Outline each blood parasite and name the species.
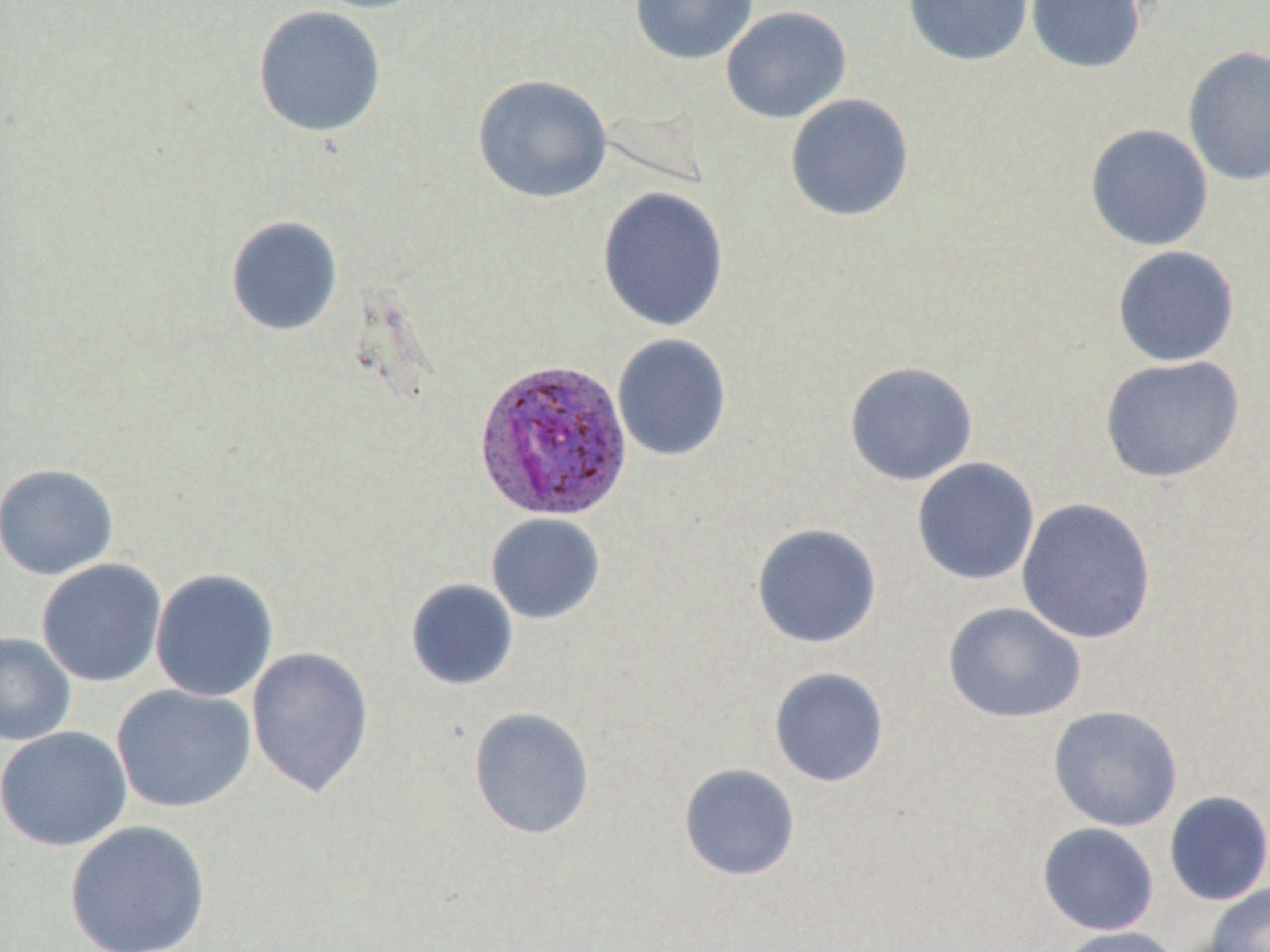
Approximate bounding boxes as [x1, y1, x2, y2] in pixels.
Plasmodium ovale-infected red blood cells: [472, 357, 635, 522].
No Plasmodium falciparum, Plasmodium malariae, Plasmodium vivax, Babesia divergens, or Trypanosoma brucei observed.

slide-level diagnosis = Plasmodium ovale
preparation = thin blood smear
magnification = 1000x
image size = 1270×952 pixels
field of view = one of a larger specimen
uninfected red blood cell locations = approximate bounding boxes as [x1, y1, x2, y2] in pixels: [306, 0, 434, 13], [630, 0, 758, 65], [903, 0, 1035, 67], [1025, 0, 1146, 74], [252, 5, 388, 138], [721, 6, 852, 124], [1183, 45, 1270, 186], [472, 73, 613, 204], [784, 93, 915, 223], [1084, 123, 1214, 252], [597, 185, 730, 332], [225, 214, 344, 337], [1112, 245, 1240, 367], [612, 333, 733, 462], [1099, 355, 1245, 483], [844, 361, 978, 486], [911, 457, 1041, 586], [0, 463, 119, 580], [1016, 497, 1157, 644], [485, 513, 606, 625], [751, 523, 882, 649], [36, 558, 167, 687], [150, 568, 279, 703], [404, 578, 520, 692], [942, 602, 1087, 724], [0, 632, 77, 746], [246, 646, 375, 798], [768, 667, 890, 788], [111, 683, 256, 813], [1048, 705, 1183, 832], [468, 707, 596, 840], [0, 725, 133, 853], [678, 763, 801, 881], [1163, 790, 1270, 906], [64, 820, 212, 952], [1037, 822, 1160, 935], [1204, 884, 1270, 952], [1056, 926, 1182, 952]
stain = May-Grünwald-Giemsa
modality = optical microscopy